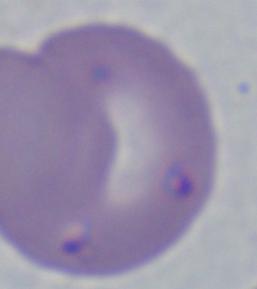
Summary:
  - Modality: micrograph
  - Identification: Babesia
  - Magnification: 1000x